Give the position of every Plasmodium parasite visible.
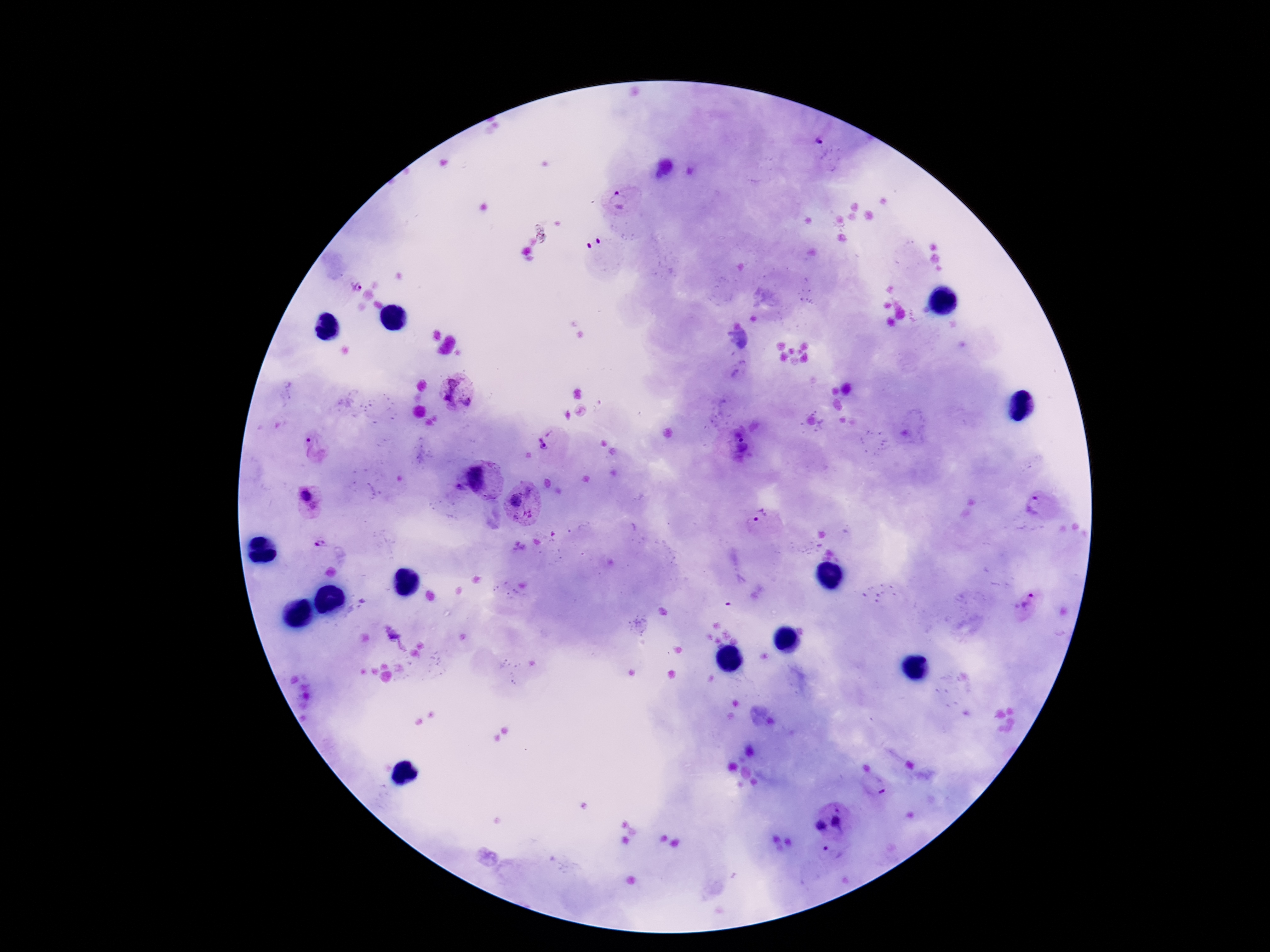
Approximate centers as [x, y] in pixels.
Plasmodium parasites: [818, 144], [623, 199], [355, 286], [458, 394], [548, 440], [313, 445], [476, 476], [308, 500], [523, 502], [1039, 507], [759, 518], [320, 546], [1027, 602], [839, 823], [821, 825].

Summary:
  - Field of view: single
  - Image size: 1270×952 pixels
  - Magnification: 100x
  - Capture: smartphone camera through the microscope eyepiece
  - Patient malaria status: infected
  - Preparation: thick blood film
  - Stain: Giemsa